Assess this cell for malaria.
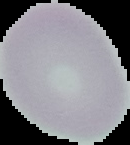
It is uninfected.

Image is 130×145 pixels. Cell region segmented out of the field of view; the surrounding area is masked to black. From a thin blood smear.